Outline white blood cells.
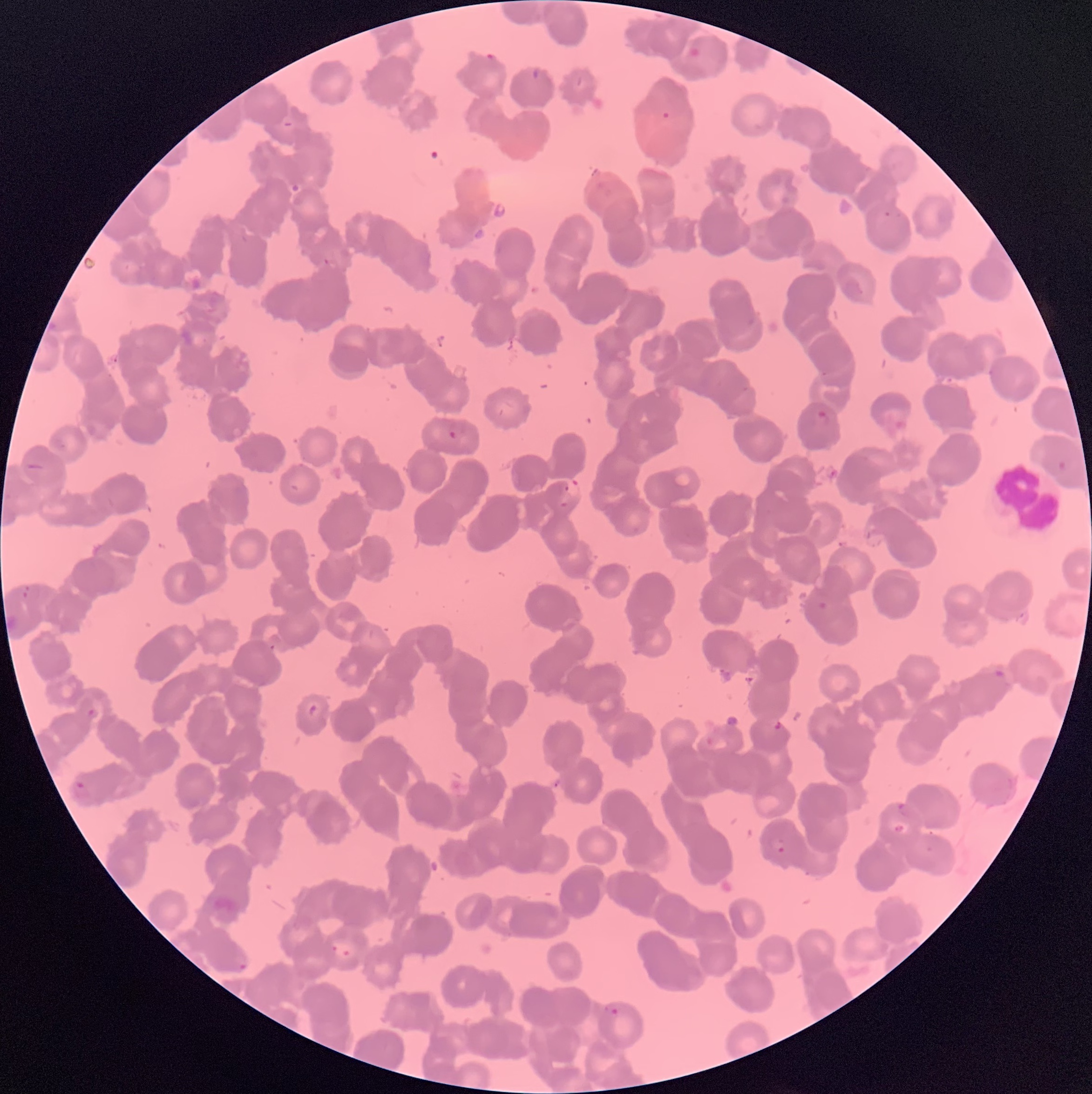

Approximate bounding boxes as (x1,y1)-(x2,y2) corner pairs in pixels.
White blood cells: (995,463)-(1060,532).

Summary:
  - Plasmodium parasites too small for a box (approximate centers as (x,y) in pixels): (824,374), (746,389), (564,504), (272,647), (91,712)
  - Plasmodium parasite locations: (485,53)-(499,62), (533,69)-(539,79), (884,208)-(903,218), (323,257)-(330,265), (49,322)-(58,331), (811,411)-(832,425), (86,416)-(112,441), (447,420)-(468,439), (53,438)-(69,448), (1051,461)-(1066,473), (26,462)-(46,471), (565,479)-(583,499), (23,583)-(42,601), (819,602)-(827,609), (995,669)-(1006,679), (310,704)-(321,719), (706,735)-(729,753), (71,780)-(91,800), (898,803)-(915,817), (893,824)-(906,834), (770,837)-(787,853), (926,845)-(933,853), (239,964)-(247,970), (604,1004)-(619,1015)
  - Image size: 1092×1094 pixels
  - Modality: optical microscopy
  - Red blood cell morphology: rouleaux formation
  - Preparation: thin blood smear